Assess this cell for malaria.
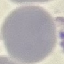
Uninfected.

Thin smear of blood. Automatically extracted cell patch, resized to 64 × 64 pixels. Giemsa-stained preparation. Acquired by smartphone through the microscope eyepiece.